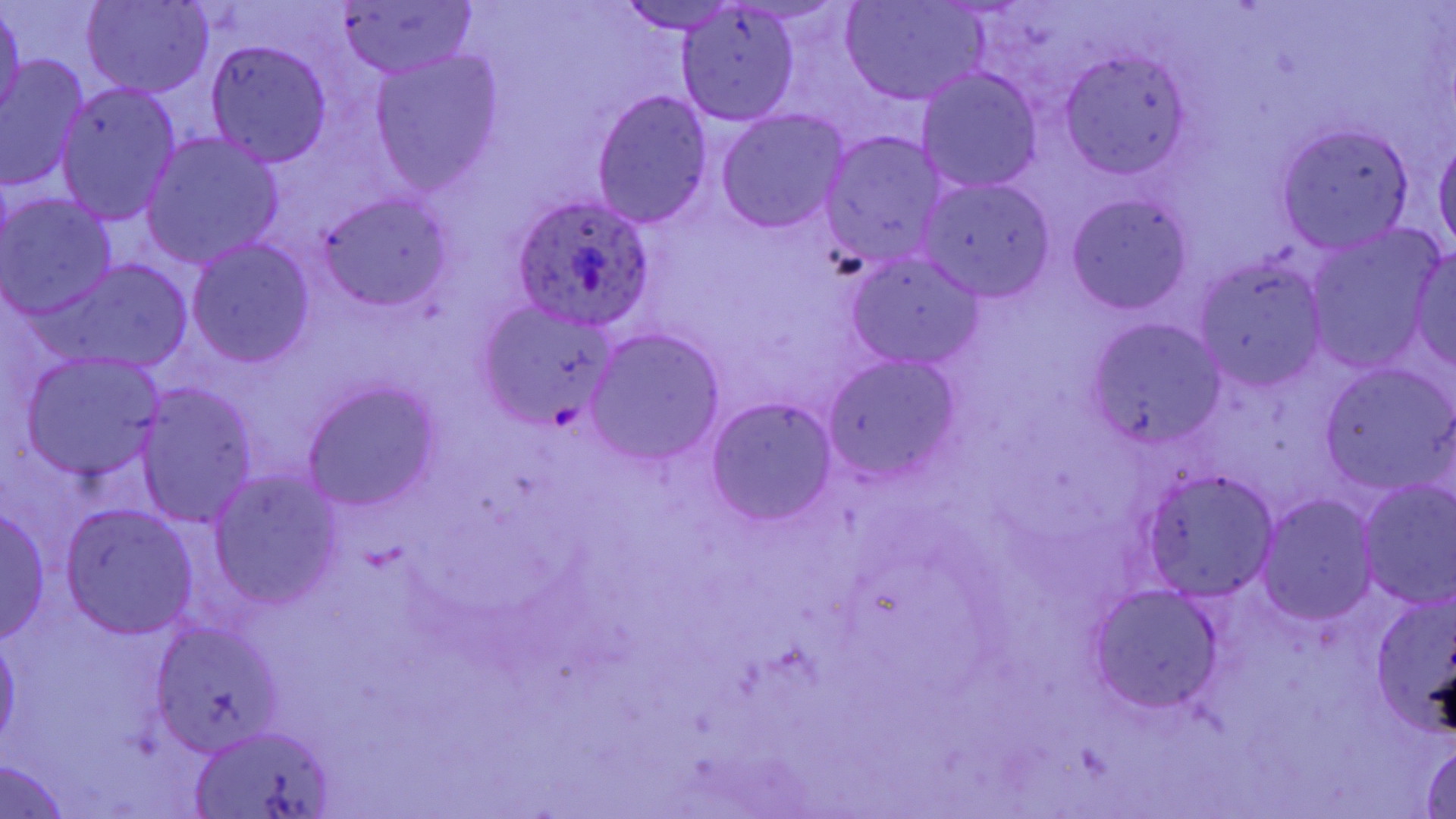 Approximate bounding boxes as (x1,y1)-(x2,y2) corner pairs in pixels. Plasmodium ovale-infected red blood cell locations: (511,197)-(659,333). Uninfected red blood cell locations: (83,0)-(213,98), (841,1)-(988,106), (0,2)-(25,127), (335,2)-(475,78), (614,2)-(743,34), (675,6)-(800,126), (206,41)-(332,166), (1060,52)-(1191,178), (371,53)-(502,191), (1,55)-(90,191), (917,67)-(1043,192), (55,81)-(183,225), (591,90)-(715,228), (716,109)-(849,235), (1280,124)-(1413,250), (820,131)-(948,270), (1434,132)-(1455,258), (143,133)-(283,267), (918,176)-(1056,300), (1,193)-(117,317), (315,194)-(455,308), (1067,194)-(1192,315), (1304,231)-(1438,371), (188,239)-(316,367), (1364,241)-(1456,371), (1409,249)-(1456,368), (845,251)-(985,370), (1195,257)-(1330,390), (51,260)-(192,369), (474,299)-(621,432), (1090,318)-(1226,454), (586,331)-(724,464), (22,354)-(168,483), (821,354)-(964,484), (1322,365)-(1453,492), (303,380)-(442,511), (135,386)-(257,526), (706,397)-(839,527), (209,470)-(344,609), (1143,470)-(1279,599), (1355,481)-(1456,607), (1257,494)-(1377,625), (0,505)-(51,644), (59,505)-(200,639), (1371,581)-(1456,741), (1087,585)-(1224,713), (152,622)-(287,755), (0,634)-(21,750), (194,729)-(334,819), (1418,739)-(1456,818), (0,759)-(75,816). Slide-level diagnosis: Plasmodium ovale. Thin blood smear. Image is 1456×819 pixels. One field of a larger specimen. May-Grünwald-Giemsa-stained preparation. Captured at 1000x magnification. Light microscopy.